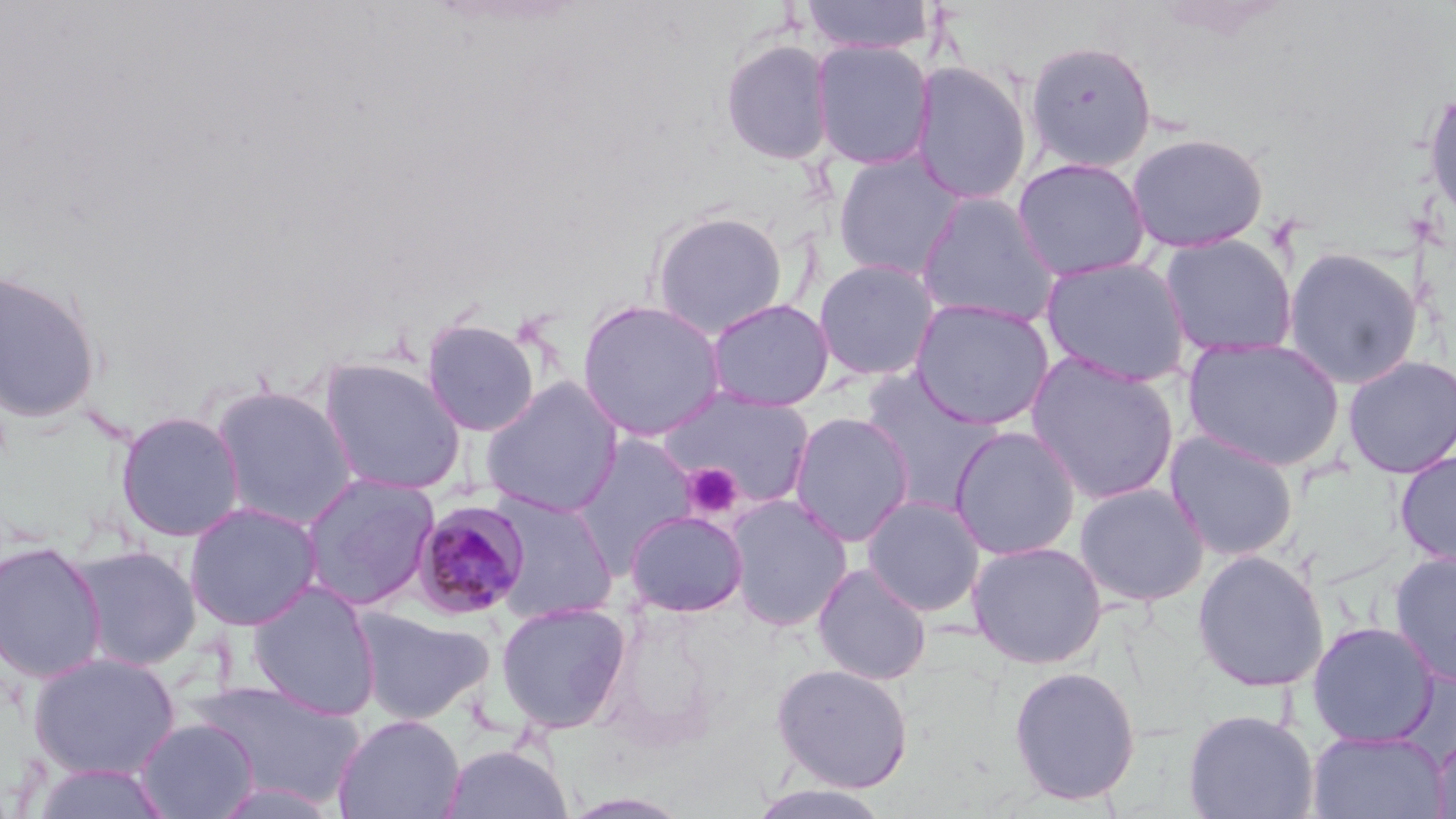
Approximate bounding boxes as (x1,y1)-(x2,y2) corner pairs in pixels. Plasmodium malariae-infected red blood cell locations: (410,501)-(531,620). Platelet locations: (682,462)-(743,519). Uninfected red blood cell locations: (800,0)-(935,56), (720,38)-(835,166), (810,40)-(934,170), (1024,40)-(1157,173), (911,61)-(1033,205), (1423,88)-(1456,228), (1126,131)-(1269,254), (831,150)-(966,281), (1012,157)-(1151,281), (915,193)-(1061,327), (649,210)-(790,339), (1159,234)-(1296,360), (1283,246)-(1423,389), (1041,256)-(1192,387), (813,258)-(941,381), (1,266)-(102,426), (909,297)-(1056,430), (577,298)-(726,442), (705,298)-(835,412), (420,317)-(543,436), (1182,336)-(1346,472), (1025,352)-(1181,504), (1342,354)-(1456,479), (317,356)-(467,495), (858,368)-(1005,511), (479,377)-(624,518), (209,384)-(359,530), (659,386)-(816,512), (116,410)-(246,542), (788,411)-(915,547), (948,425)-(1082,560), (1164,429)-(1299,562), (572,434)-(699,569), (1394,451)-(1456,568), (298,471)-(441,611), (1073,482)-(1209,606), (487,492)-(619,623), (725,494)-(853,631), (862,495)-(986,616), (183,501)-(323,632), (625,509)-(749,617), (0,540)-(107,683), (967,540)-(1108,668), (68,544)-(203,671), (1191,550)-(1329,692), (1389,551)-(1456,687), (812,563)-(932,686), (246,581)-(381,720), (494,601)-(631,734), (350,607)-(493,726), (1307,621)-(1439,747), (27,651)-(182,780), (771,662)-(914,793), (1008,665)-(1142,806), (187,677)-(365,809), (1182,708)-(1320,819), (332,714)-(465,819), (133,718)-(259,819), (1307,728)-(1447,819), (1430,731)-(1456,819), (440,743)-(573,819), (30,761)-(172,819), (210,780)-(340,819), (746,784)-(894,819). Slide-level diagnosis: Plasmodium malariae. Thin blood smear. May-Grünwald-Giemsa stain. Image is 1456×819 pixels. Light microscopy. Single field of view. Captured at 1000x magnification.